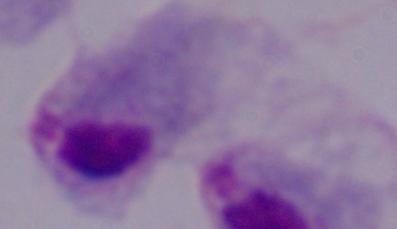

Summary:
  - Magnification: 1000x
  - Identification: trichomonad
  - Modality: micrograph